Report the malaria status of this cell.
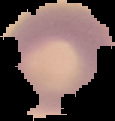

It is uninfected.

Summary:
  - Image type: segmented cell region on a black background
  - Image size: 115×121 pixels
  - Preparation: thin blood smear